Give the position of every Plasmodium parasite visible.
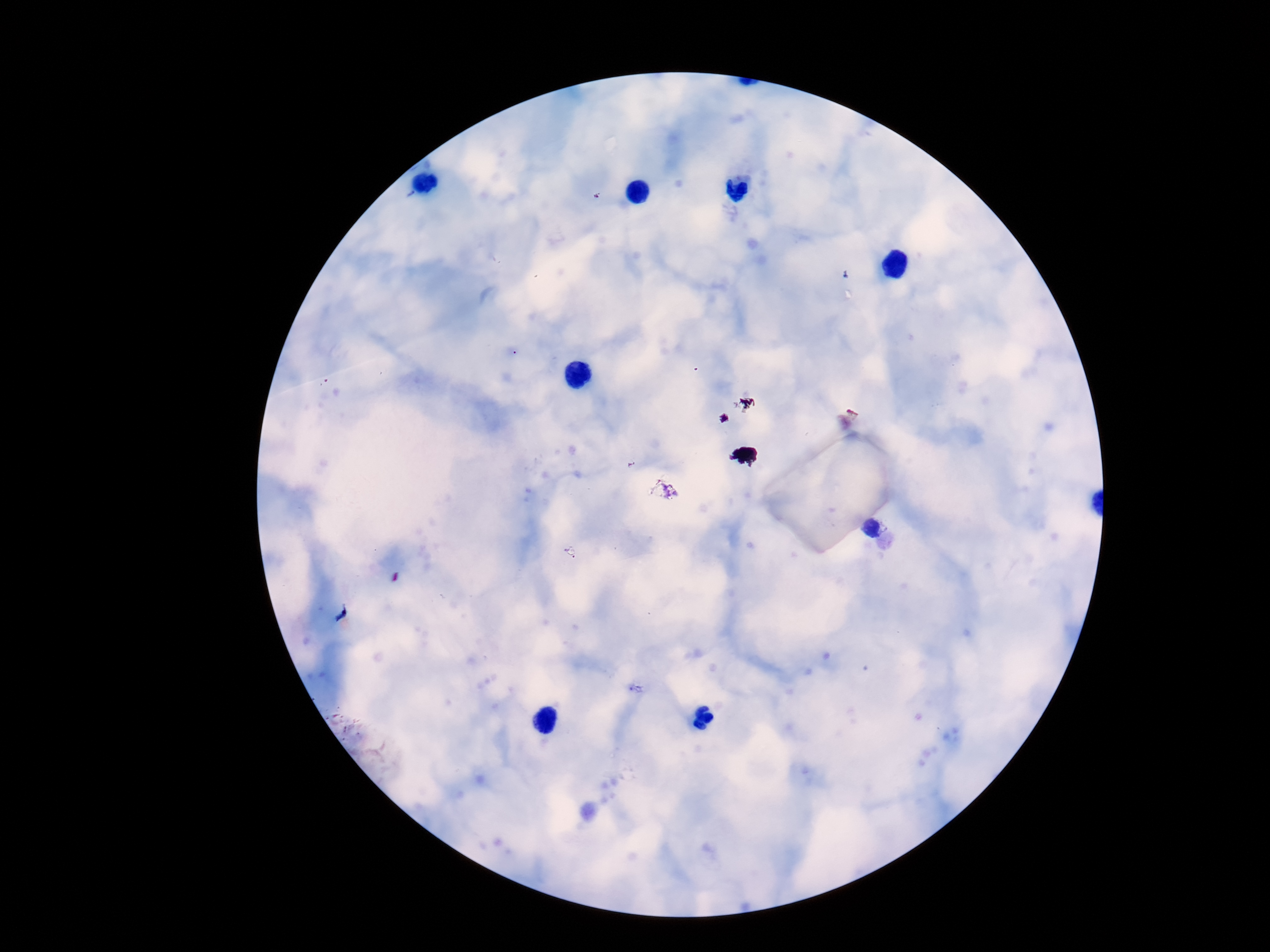

Approximate centers as {x, y} in pixels.
Plasmodium parasites: {664, 493}, {874, 528}.

Summary:
  - Field of view: one from this slide
  - Magnification: 100x
  - Preparation: thick peripheral-blood smear
  - Image size: 1270×952 pixels
  - Stain: Giemsa
  - Capture: smartphone camera through the microscope eyepiece
  - Patient malaria status: infected